Give the extent of all Plasmodium ovale-infected red blood cells.
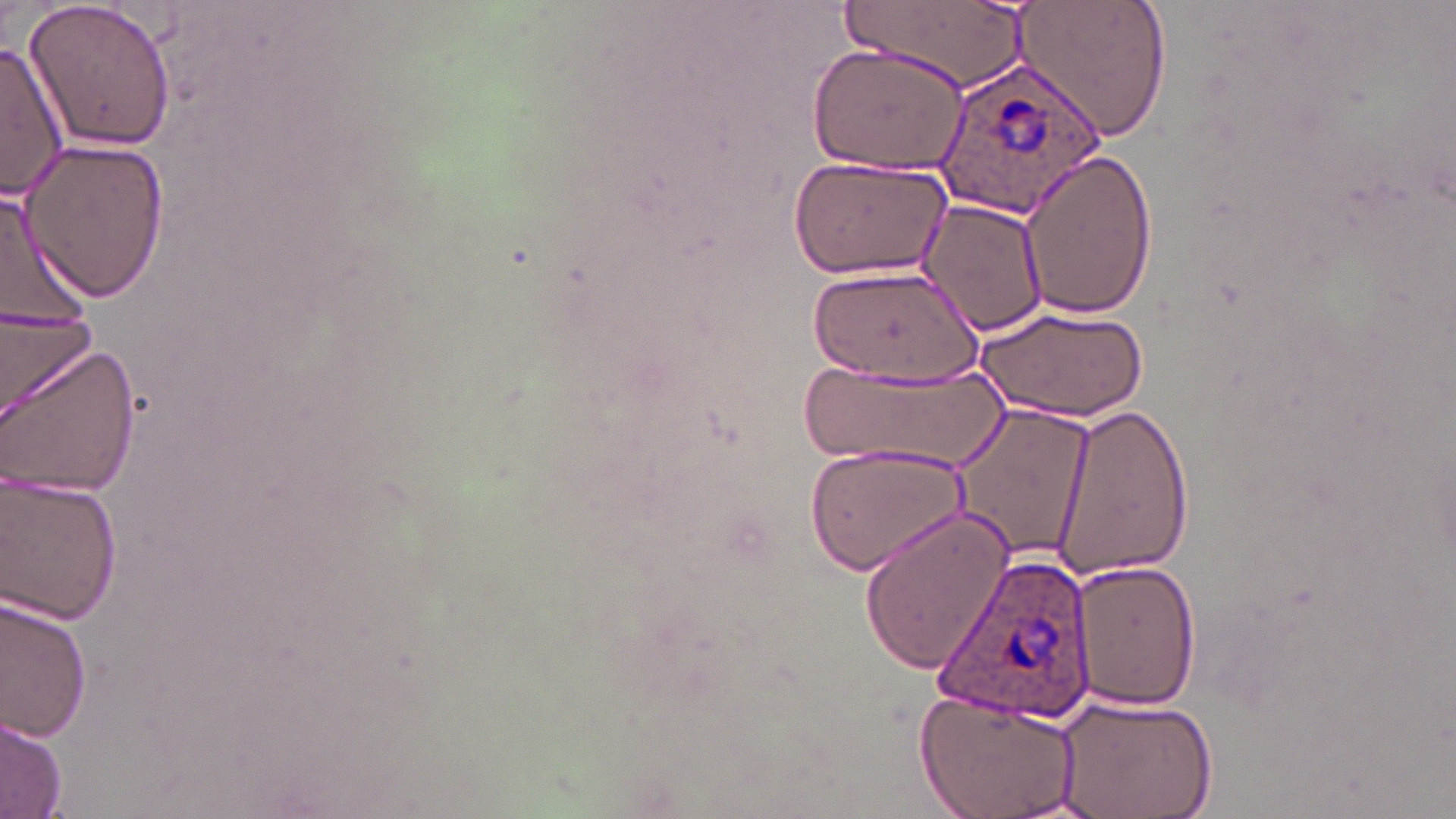

Approximate bounding boxes as named x1/y1/x2/y2 corners in pixels.
Plasmodium ovale-infected red blood cells: (x1=935, y1=63, x2=1103, y2=222), (x1=930, y1=552, x2=1098, y2=724).

Summary:
  - Uninfected red blood cell locations: (x1=22, y1=0, x2=179, y2=155), (x1=845, y1=0, x2=1029, y2=88), (x1=1012, y1=0, x2=1172, y2=148), (x1=808, y1=42, x2=970, y2=175), (x1=0, y1=43, x2=68, y2=201), (x1=20, y1=138, x2=170, y2=303), (x1=1019, y1=148, x2=1162, y2=319), (x1=788, y1=155, x2=954, y2=279), (x1=0, y1=179, x2=100, y2=358), (x1=918, y1=199, x2=1048, y2=339), (x1=809, y1=264, x2=982, y2=391), (x1=0, y1=298, x2=100, y2=422), (x1=975, y1=303, x2=1151, y2=422), (x1=2, y1=340, x2=141, y2=504), (x1=794, y1=359, x2=1006, y2=470), (x1=950, y1=402, x2=1099, y2=563), (x1=1051, y1=403, x2=1198, y2=580), (x1=803, y1=438, x2=972, y2=578), (x1=0, y1=470, x2=123, y2=625), (x1=858, y1=507, x2=1017, y2=675), (x1=1070, y1=557, x2=1199, y2=712), (x1=1, y1=592, x2=94, y2=747), (x1=913, y1=687, x2=1084, y2=819), (x1=1050, y1=690, x2=1217, y2=819), (x1=1, y1=715, x2=69, y2=816)
  - Slide-level diagnosis: Plasmodium ovale
  - Image size: 1456×819 pixels
  - Stain: May-Grünwald-Giemsa
  - Field of view: single
  - Modality: light microscopy
  - Magnification: 1000x
  - Preparation: thin blood film